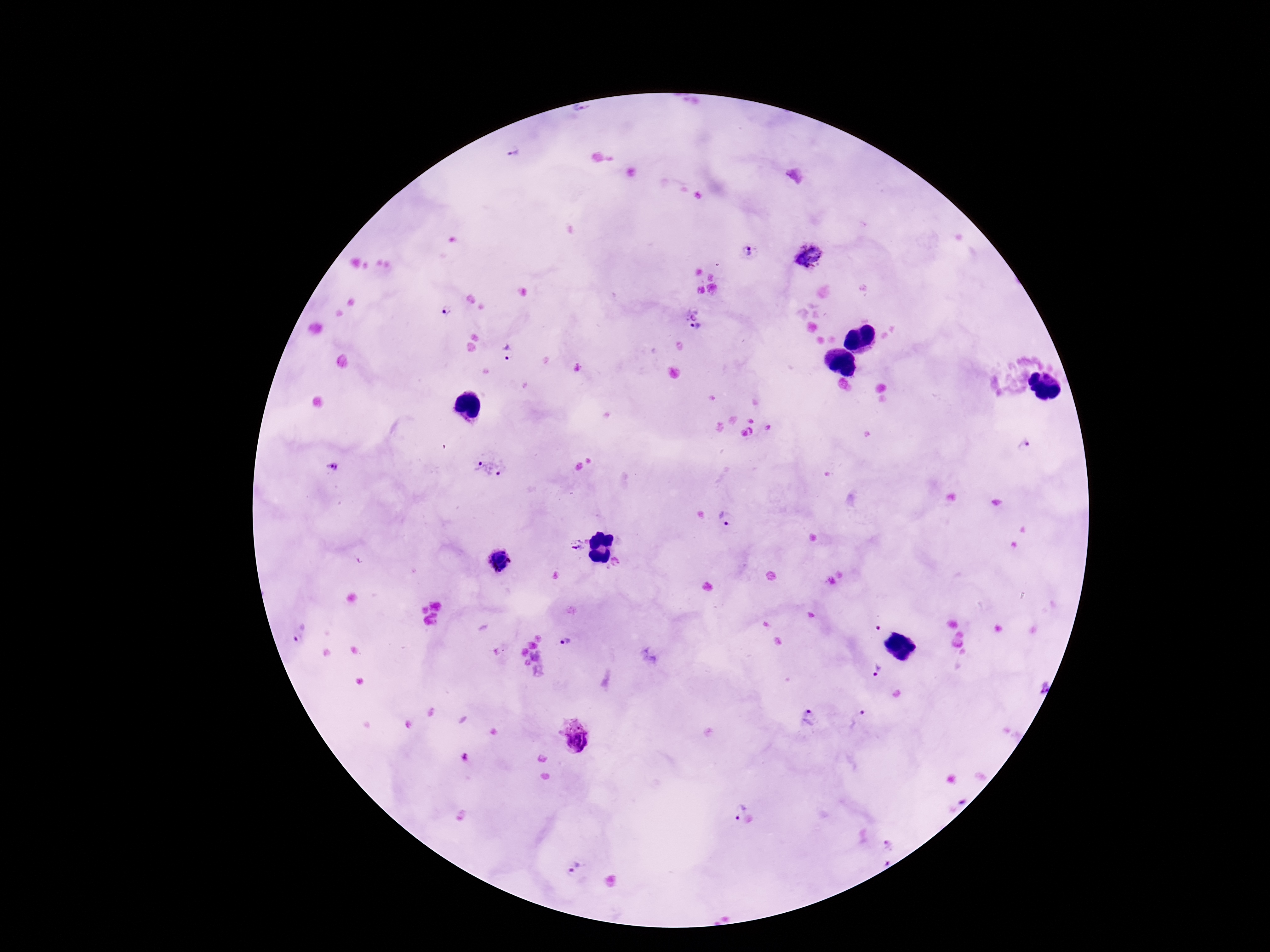

{
  "plasmodium_parasite_locations": "approximate centers as [x, y] in pixels: [581, 109], [514, 152], [749, 252], [810, 256], [448, 310], [692, 314], [695, 327], [507, 353], [1023, 446], [333, 466], [489, 469], [726, 520], [577, 544], [501, 560], [616, 563], [877, 629], [297, 636], [566, 642], [876, 670], [1042, 686], [810, 718], [860, 719], [574, 736], [465, 759], [737, 809], [887, 844], [886, 862], [575, 865]",
  "image_size": "1270×952 pixels",
  "magnification": "100x",
  "capture": "smartphone camera through the microscope eyepiece",
  "stain": "Giemsa",
  "patient_malaria_status": "positive",
  "preparation": "thick peripheral-blood smear",
  "field_of_view": "one from this slide"
}